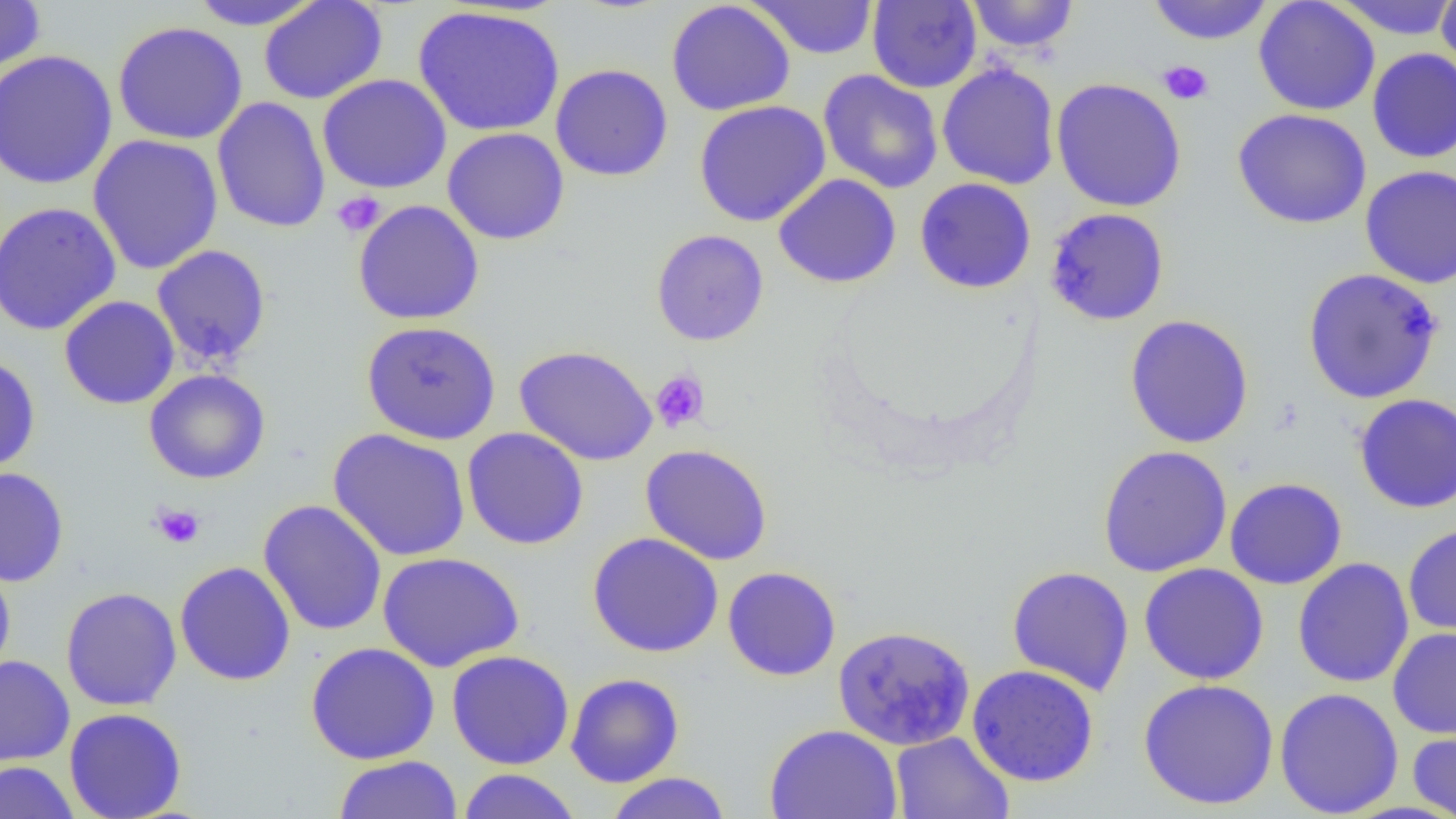

Approximate bounding boxes as named x1/y1/x2/y2 corners in pixels. Uninfected red blood cell locations: (x1=185, y1=0, x2=324, y2=29), (x1=258, y1=0, x2=388, y2=104), (x1=666, y1=0, x2=795, y2=117), (x1=966, y1=0, x2=1080, y2=53), (x1=1146, y1=0, x2=1275, y2=45), (x1=1253, y1=0, x2=1380, y2=116), (x1=1329, y1=0, x2=1456, y2=40), (x1=1436, y1=0, x2=1456, y2=82), (x1=0, y1=1, x2=46, y2=75), (x1=748, y1=1, x2=879, y2=60), (x1=867, y1=1, x2=982, y2=93), (x1=413, y1=5, x2=566, y2=138), (x1=113, y1=21, x2=248, y2=145), (x1=1367, y1=48, x2=1456, y2=163), (x1=0, y1=50, x2=118, y2=190), (x1=937, y1=62, x2=1060, y2=190), (x1=550, y1=63, x2=673, y2=182), (x1=818, y1=69, x2=943, y2=194), (x1=317, y1=74, x2=452, y2=194), (x1=1050, y1=78, x2=1187, y2=212), (x1=212, y1=96, x2=331, y2=234), (x1=694, y1=100, x2=831, y2=227), (x1=1232, y1=108, x2=1372, y2=229), (x1=442, y1=127, x2=570, y2=245), (x1=87, y1=134, x2=224, y2=275), (x1=1360, y1=165, x2=1456, y2=288), (x1=773, y1=173, x2=901, y2=288), (x1=914, y1=177, x2=1036, y2=294), (x1=352, y1=199, x2=485, y2=326), (x1=0, y1=201, x2=122, y2=336), (x1=1044, y1=207, x2=1170, y2=326), (x1=650, y1=228, x2=769, y2=346), (x1=151, y1=244, x2=272, y2=367), (x1=1302, y1=267, x2=1443, y2=404), (x1=58, y1=295, x2=180, y2=409), (x1=1124, y1=314, x2=1255, y2=449), (x1=360, y1=320, x2=501, y2=445), (x1=514, y1=345, x2=658, y2=466), (x1=0, y1=355, x2=41, y2=476), (x1=144, y1=369, x2=271, y2=484), (x1=1353, y1=393, x2=1456, y2=513), (x1=462, y1=427, x2=589, y2=550), (x1=328, y1=428, x2=471, y2=562), (x1=640, y1=444, x2=773, y2=565), (x1=1097, y1=445, x2=1233, y2=577), (x1=0, y1=467, x2=69, y2=586), (x1=1224, y1=477, x2=1347, y2=590), (x1=258, y1=499, x2=387, y2=636), (x1=1403, y1=523, x2=1456, y2=639), (x1=587, y1=532, x2=724, y2=657), (x1=378, y1=551, x2=524, y2=672), (x1=0, y1=556, x2=16, y2=681), (x1=1293, y1=557, x2=1414, y2=688), (x1=175, y1=561, x2=295, y2=686), (x1=1139, y1=563, x2=1269, y2=685), (x1=1007, y1=565, x2=1135, y2=696), (x1=722, y1=566, x2=841, y2=681), (x1=60, y1=586, x2=182, y2=711), (x1=832, y1=624, x2=975, y2=751), (x1=1388, y1=627, x2=1456, y2=739), (x1=305, y1=642, x2=440, y2=764), (x1=447, y1=650, x2=575, y2=770), (x1=0, y1=655, x2=75, y2=766), (x1=967, y1=664, x2=1099, y2=787), (x1=565, y1=672, x2=684, y2=787), (x1=1138, y1=678, x2=1279, y2=810), (x1=1274, y1=687, x2=1404, y2=817), (x1=64, y1=708, x2=187, y2=818), (x1=764, y1=723, x2=903, y2=819), (x1=1407, y1=727, x2=1456, y2=819), (x1=890, y1=731, x2=1014, y2=819), (x1=333, y1=755, x2=463, y2=819), (x1=0, y1=761, x2=81, y2=819), (x1=457, y1=768, x2=580, y2=819), (x1=604, y1=772, x2=732, y2=819). Platelet locations: (x1=1157, y1=60, x2=1213, y2=105), (x1=331, y1=191, x2=386, y2=237), (x1=650, y1=369, x2=710, y2=433), (x1=152, y1=503, x2=205, y2=549). Slide-level diagnosis: no evidence of blood parasites. Image is 1456×819 pixels. Thin blood film. 1000x magnification. Light microscopy. One field of a larger specimen.